Identify the blood parasite species.
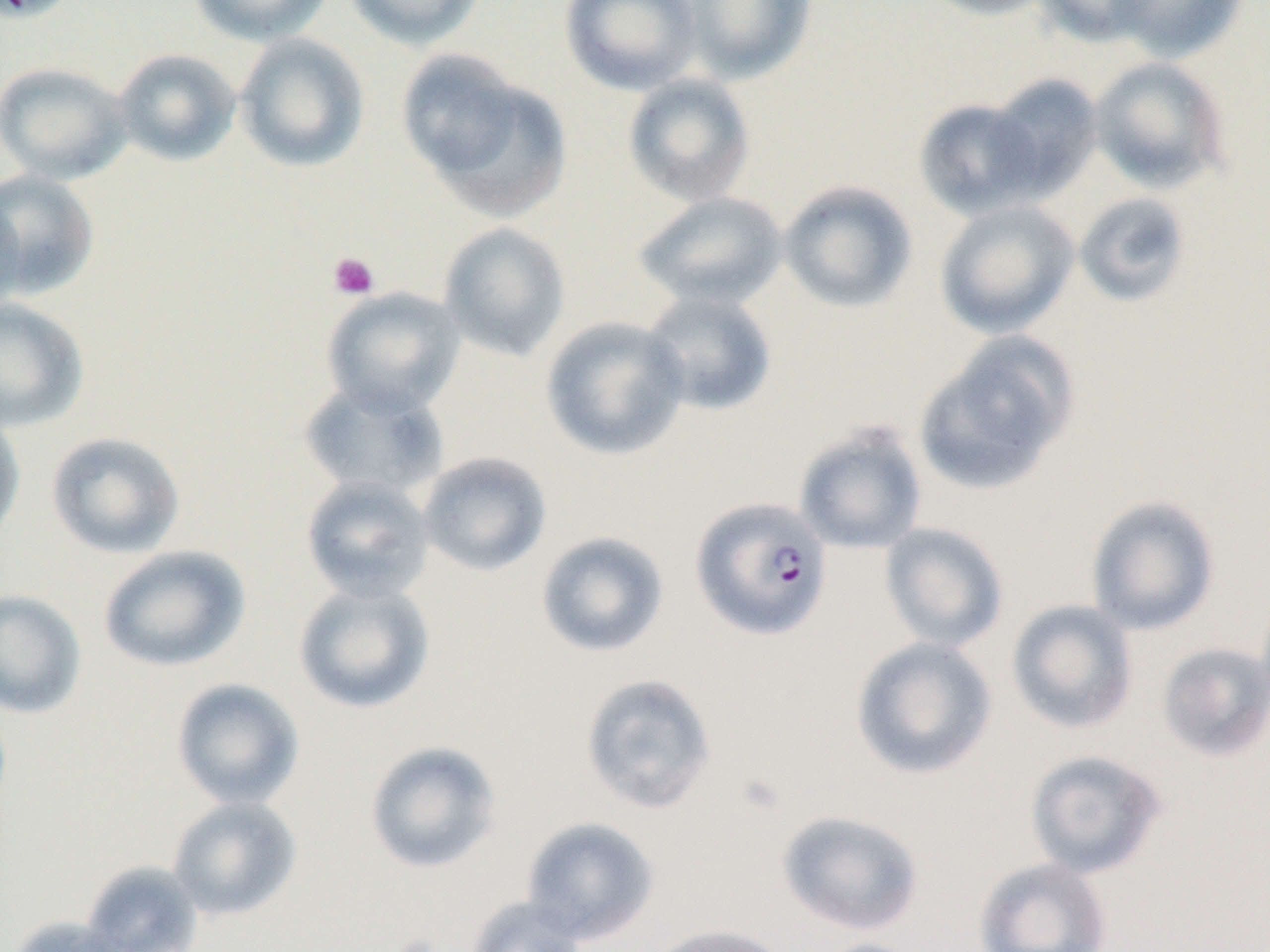
Plasmodium falciparum.

Approximate bounding boxes as [x1, y1, x2, y2] in pixels. Uninfected red blood cell locations: [0, 0, 80, 23], [189, 0, 334, 46], [344, 0, 485, 49], [560, 0, 702, 95], [675, 0, 817, 84], [917, 0, 1060, 21], [1034, 0, 1160, 48], [1108, 0, 1247, 62], [234, 32, 371, 173], [112, 48, 241, 167], [400, 53, 571, 223], [1088, 56, 1231, 193], [0, 61, 134, 185], [622, 72, 756, 207], [984, 73, 1103, 199], [914, 97, 1047, 220], [0, 169, 101, 300], [778, 180, 918, 314], [633, 191, 789, 311], [1073, 192, 1193, 308], [0, 193, 28, 319], [934, 200, 1080, 340], [438, 222, 571, 361], [321, 286, 465, 416], [638, 289, 778, 417], [0, 297, 90, 433], [540, 315, 691, 461], [913, 332, 1079, 498], [298, 378, 450, 501], [0, 413, 26, 549], [794, 421, 928, 555], [45, 431, 186, 559], [418, 451, 552, 576], [300, 475, 435, 603], [1085, 495, 1221, 636], [879, 522, 1009, 652], [536, 530, 669, 658], [97, 545, 251, 673], [293, 579, 436, 714], [0, 588, 87, 719], [1006, 599, 1138, 735], [850, 635, 998, 781], [1156, 642, 1270, 762], [580, 672, 717, 815], [171, 678, 305, 810], [364, 741, 501, 874], [1023, 749, 1167, 879], [167, 796, 302, 921], [776, 809, 926, 936], [521, 816, 659, 944], [973, 856, 1113, 952], [79, 861, 203, 952], [464, 895, 589, 952], [8, 915, 137, 952], [646, 923, 792, 952], [806, 938, 927, 952]. Plasmodium falciparum-infected red blood cell locations: [690, 496, 834, 640]. Platelet locations: [328, 251, 380, 301], [733, 772, 788, 816]. Thin blood film. Captured at 1000x magnification. One field of a larger specimen. Image is 1270×952 pixels. Light microscopy.